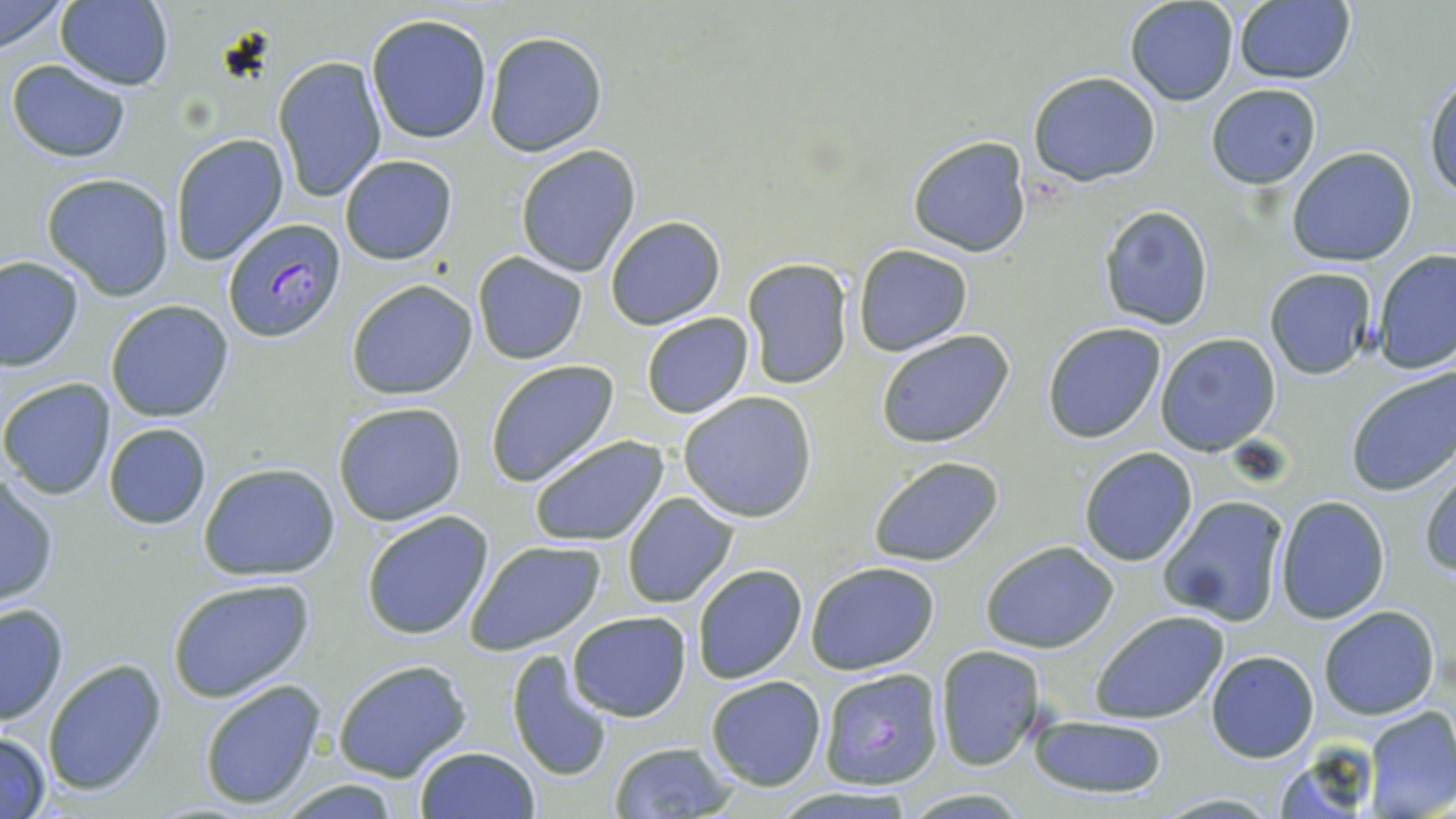

Approximate bounding boxes as (x1, y1, x2, y2) in pixels. Uninfected red blood cell locations: (1, 0, 69, 54), (1123, 0, 1238, 105), (55, 1, 174, 89), (1232, 2, 1356, 85), (367, 14, 492, 143), (482, 31, 607, 157), (272, 54, 387, 204), (6, 58, 133, 164), (1424, 70, 1456, 202), (1029, 72, 1160, 185), (1206, 83, 1323, 188), (169, 132, 289, 265), (907, 134, 1032, 257), (515, 146, 641, 277), (1286, 146, 1418, 267), (339, 154, 457, 265), (42, 173, 176, 299), (1098, 204, 1215, 330), (603, 215, 725, 330), (853, 244, 972, 356), (1371, 250, 1456, 375), (472, 252, 589, 364), (1, 257, 82, 371), (740, 257, 853, 390), (1263, 266, 1378, 379), (347, 279, 477, 400), (105, 301, 234, 422), (641, 312, 754, 419), (1042, 321, 1167, 442), (876, 328, 1014, 448), (1155, 332, 1281, 456), (484, 358, 620, 488), (1345, 365, 1456, 497), (0, 378, 116, 500), (679, 391, 819, 522), (333, 402, 467, 527), (102, 423, 213, 529), (529, 434, 670, 547), (1078, 447, 1198, 566), (867, 457, 1005, 567), (199, 461, 340, 582), (1420, 466, 1456, 580), (1, 474, 60, 606), (621, 493, 738, 609), (1160, 494, 1290, 626), (1276, 495, 1390, 624), (361, 511, 495, 641), (464, 539, 605, 654), (980, 539, 1120, 653), (805, 562, 941, 676), (693, 565, 807, 684), (166, 576, 315, 701), (0, 600, 72, 726), (1318, 605, 1440, 720), (1090, 609, 1231, 725), (566, 611, 692, 721), (935, 645, 1045, 769), (506, 650, 616, 783), (1205, 650, 1319, 762), (41, 658, 167, 797), (332, 658, 472, 781), (704, 675, 827, 791), (198, 678, 327, 811), (1363, 706, 1456, 818), (1030, 713, 1169, 801), (0, 730, 52, 817), (607, 741, 739, 817), (413, 746, 539, 819), (275, 779, 402, 816), (1154, 792, 1283, 818). Plasmodium falciparum-infected red blood cell locations: (220, 217, 347, 343), (819, 668, 946, 789). Slide-level diagnosis: Plasmodium falciparum. Captured at 1000x magnification. Thin blood film. Single field of view. Light microscopy. Image is 1456×819 pixels. May-Grünwald-Giemsa stain.